Comment on the morphology of the red blood cells.
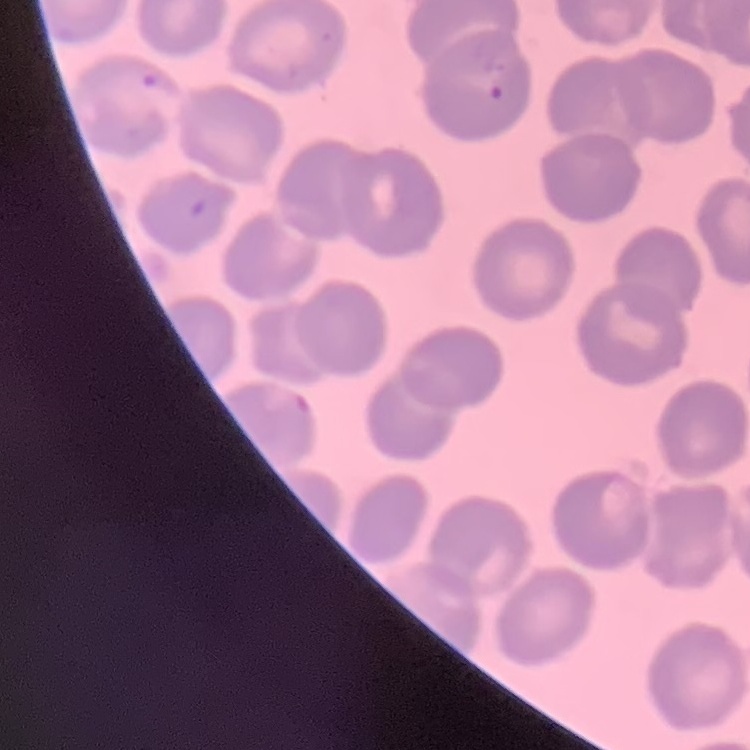
They show no rouleaux formation.

One tile cut from a larger photomicrograph. Field's or Giemsa stain. Thin peripheral smear.